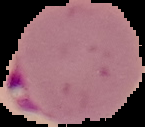
Summary:
  - Image type: segmented cell region on a black background
  - Result: Plasmodium parasites detected
  - Preparation: thin blood smear
  - Image size: 145×127 pixels